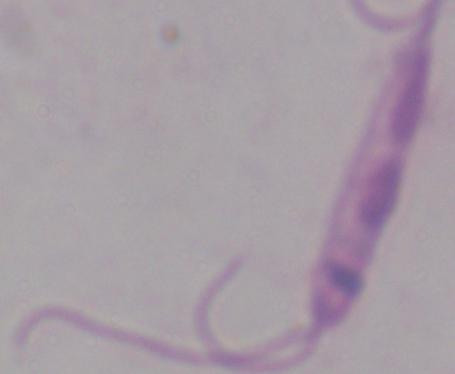

Summary:
  - Modality: micrograph
  - Identification: Leishmania
  - Magnification: 1000x